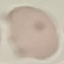
Summary:
  - Result: no malaria parasites seen
  - Image type: cell patch, automatically extracted from a larger field of view and resized to 64 × 64 pixels
  - Preparation: thin blood smear
  - Capture: smartphone camera at the microscope eyepiece
  - Stain: Giemsa